Assess this cell for malaria.
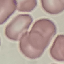

Uninfected.

stain = Giemsa
preparation = thin blood smear
image type = cell patch, automatically extracted from a larger field of view and resized to 64 × 64 pixels
capture = smartphone through the microscope eyepiece